Point out every Plasmodium parasite.
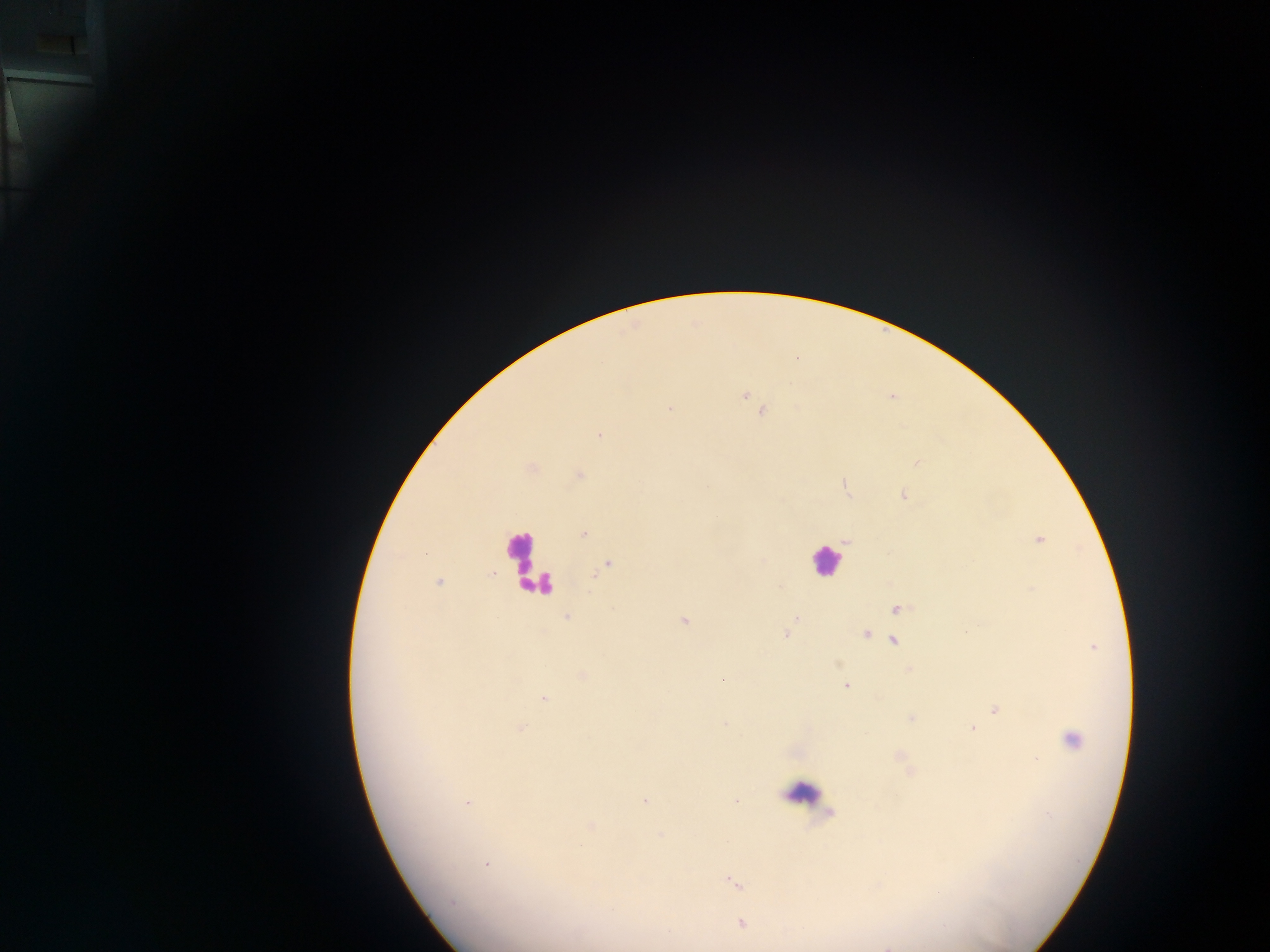

Approximate centers as {x, y} in pixels.
Plasmodium parasites: {744, 396}, {670, 409}, {762, 412}, {599, 436}, {917, 463}, {580, 475}, {845, 486}, {903, 495}, {584, 533}, {847, 540}, {1039, 541}, {606, 566}, {439, 581}, {1033, 589}, {898, 609}, {567, 617}, {795, 618}, {684, 620}, {790, 626}, {786, 634}, {865, 634}, {894, 640}, {723, 680}, {845, 685}, {544, 699}, {995, 709}, {910, 717}, {520, 729}, {972, 729}, {1071, 741}, {645, 801}, {468, 802}, {736, 802}, {591, 827}, {487, 864}, {733, 882}, {452, 903}, {741, 923}.

country = Ghana
field of view = single
capture = mobile-phone photograph through a microscope
image size = 1270×952 pixels
preparation = thick blood smear
leukocyte locations = approximate centers as {x, y} in pixels: {524, 559}, {825, 561}, {802, 793}